Locate every Plasmodium malariae-infected red blood cell.
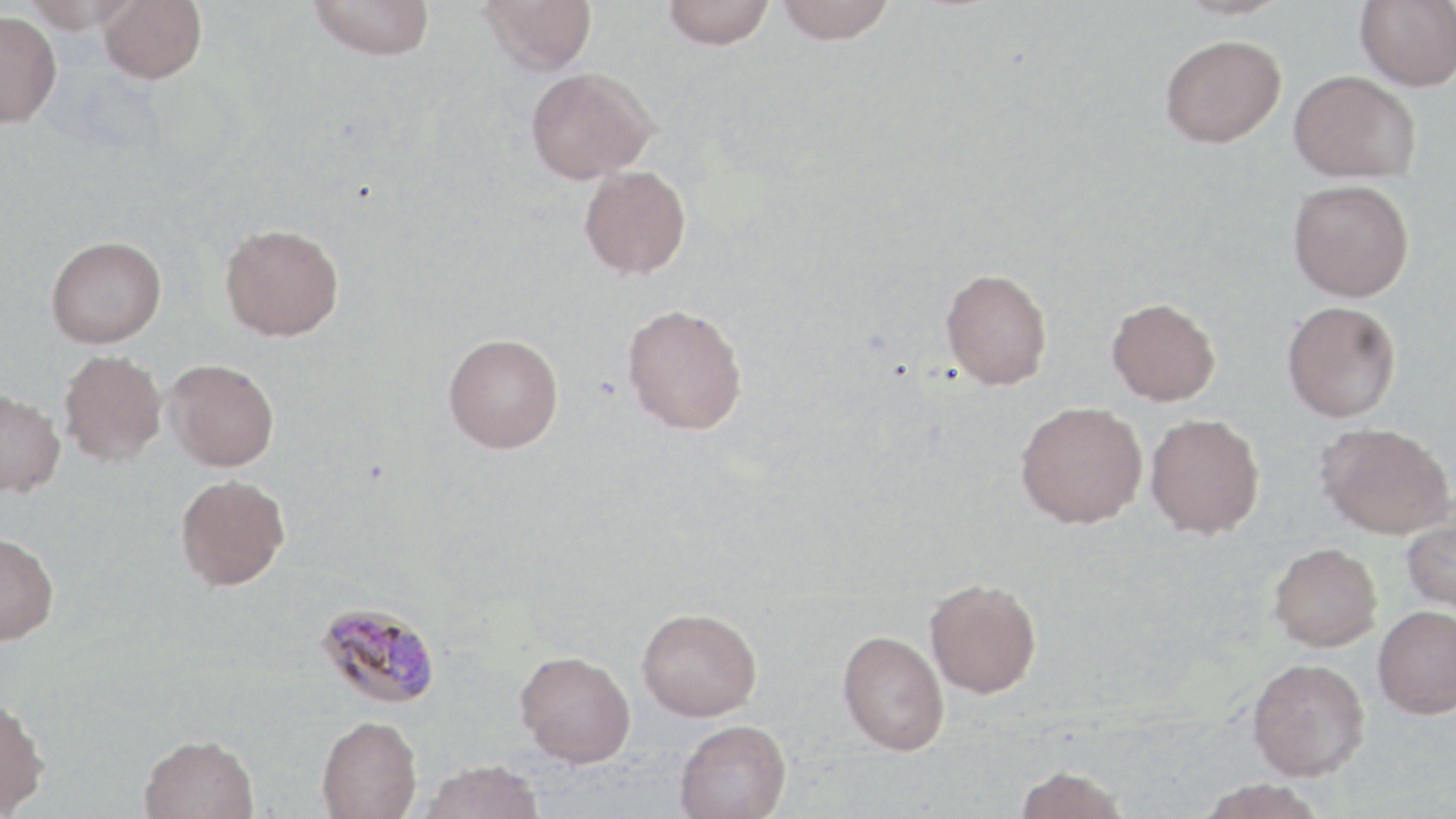
Approximate bounding boxes as (x1, y1, x2, y2) in pixels.
Plasmodium malariae-infected red blood cells: (314, 601, 442, 711).

Uninfected red blood cell locations: (20, 0, 142, 33), (98, 0, 207, 84), (307, 0, 436, 61), (478, 0, 598, 76), (662, 0, 775, 50), (775, 0, 897, 45), (1174, 0, 1293, 20), (1356, 0, 1456, 91), (0, 10, 61, 128), (1160, 34, 1286, 148), (525, 66, 658, 184), (1288, 70, 1420, 183), (579, 165, 692, 280), (1288, 179, 1414, 302), (220, 223, 344, 341), (45, 235, 167, 348), (940, 268, 1052, 389), (1106, 297, 1221, 406), (1282, 300, 1401, 422), (623, 303, 747, 435), (443, 333, 563, 453), (58, 351, 167, 466), (164, 359, 279, 471), (0, 388, 65, 498), (1016, 401, 1147, 528), (1146, 414, 1265, 539), (1317, 422, 1455, 539), (175, 474, 290, 591), (1402, 514, 1456, 615), (0, 531, 59, 645), (1268, 542, 1383, 652), (924, 577, 1042, 698), (1373, 605, 1456, 718), (637, 607, 762, 721), (838, 630, 949, 756), (515, 650, 636, 767), (1247, 657, 1370, 780), (0, 695, 50, 817), (316, 715, 422, 819), (675, 718, 792, 819), (138, 733, 260, 819), (417, 759, 546, 818), (1014, 765, 1130, 819), (1196, 778, 1332, 819). Slide-level diagnosis: Plasmodium malariae. Single field of view. Thin blood film. 1000x magnification. May-Grünwald-Giemsa-stained preparation. Optical microscopy. Image is 1456×819 pixels.